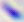

modality = photomicrograph
identification = Toxoplasma gondii
magnification = 400x